Name the parasite shown.
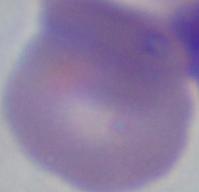

Babesia.

{
  "modality": "photomicrograph",
  "magnification": "1000x"
}